Report the malaria status of this cell.
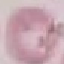
It is uninfected.

Thin blood smear. Cell patch, automatically extracted from a larger field of view and resized to 64 × 64 pixels. Giemsa stain. Photographed with a smartphone camera at the microscope eyepiece.